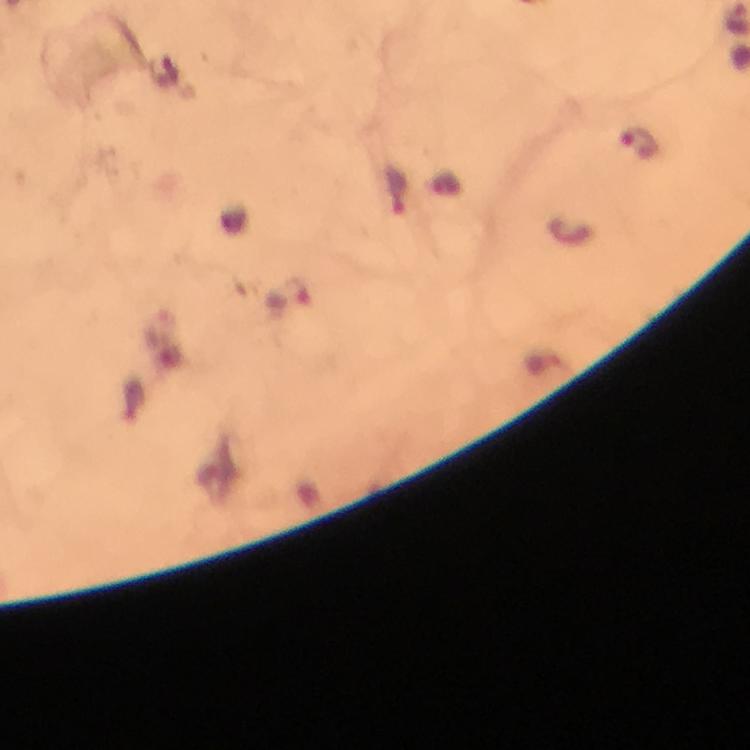
Approximate object centers, in pixels from the top-left corner. Malaria parasite locations: (x=640, y=144), (x=396, y=194), (x=290, y=297). Giemsa stain. A crop from one field of view. Thick blood film. Immersion oil applied. Image is 750×750 pixels. Smartphone photograph taken through a microscope. At 100x magnification. From a diagnostic examination for malaria.